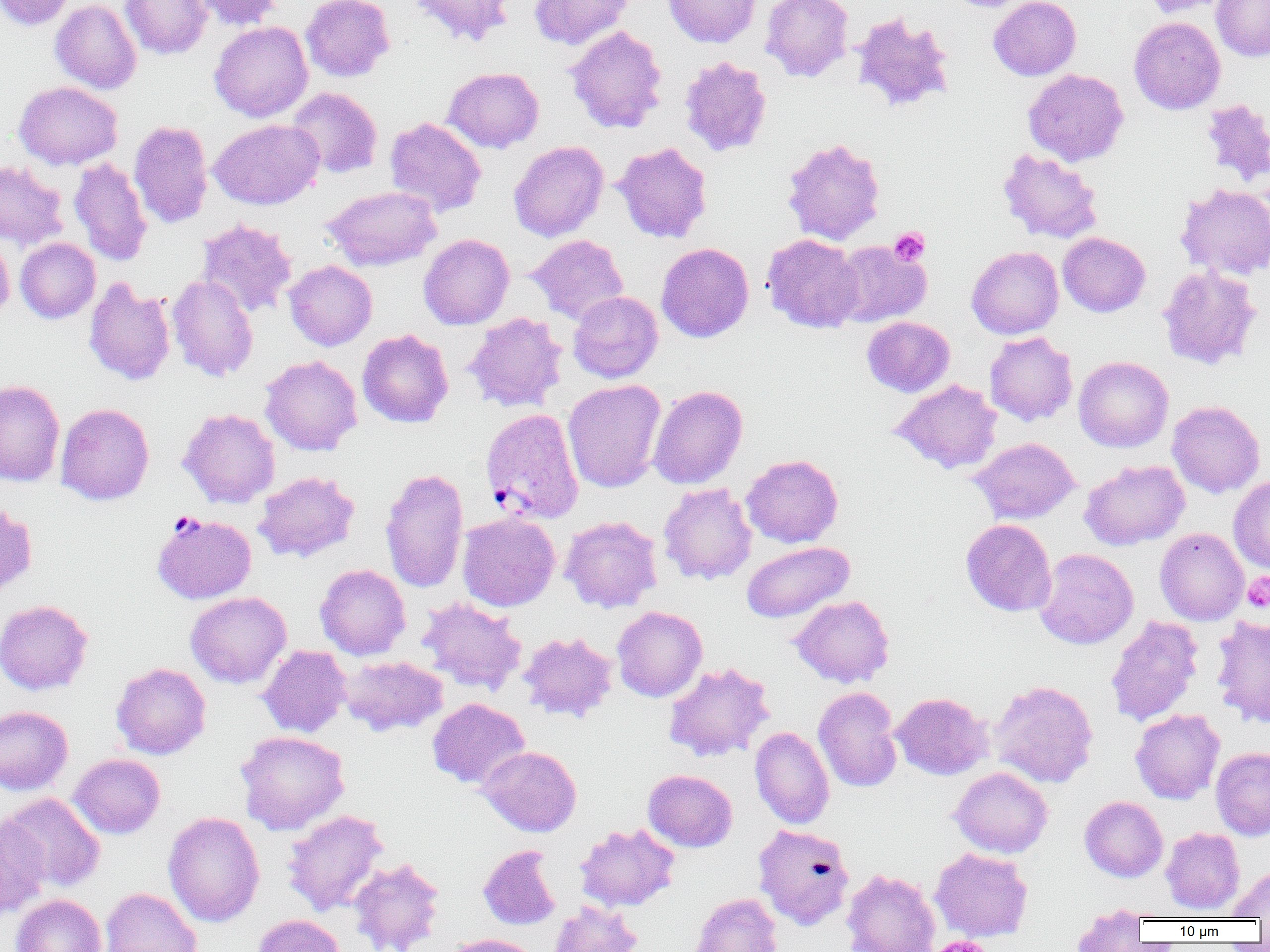

Summary:
  - Coordinate format: approximate bounding boxes as (x1, y1, x2, y2) in pixels
  - Plasmodium vivax-infected red blood cell locations: (480, 407, 585, 524), (151, 512, 257, 604)
  - Uninfected red blood cell locations: (1, 0, 76, 30), (50, 0, 142, 93), (120, 0, 212, 60), (190, 0, 284, 30), (300, 0, 395, 82), (408, 0, 514, 47), (529, 0, 636, 50), (663, 0, 761, 48), (761, 0, 854, 81), (948, 0, 1031, 12), (989, 0, 1081, 80), (1141, 0, 1233, 18), (1211, 0, 1270, 61), (851, 12, 956, 114), (1129, 16, 1226, 114), (209, 21, 313, 122), (565, 25, 668, 134), (679, 56, 772, 157), (443, 67, 544, 153), (1023, 69, 1128, 166), (14, 81, 123, 170), (287, 87, 383, 178), (1200, 98, 1270, 188), (384, 117, 486, 217), (209, 119, 324, 209), (129, 120, 213, 228), (782, 138, 886, 245), (509, 141, 609, 242), (612, 141, 712, 243), (997, 148, 1103, 244), (69, 157, 153, 265), (0, 160, 68, 250), (1176, 184, 1270, 280), (322, 186, 441, 271), (196, 218, 297, 318), (0, 232, 14, 324), (1058, 232, 1151, 317), (419, 233, 514, 329), (527, 234, 629, 324), (762, 234, 863, 333), (15, 238, 100, 323), (831, 240, 931, 328), (656, 242, 754, 342), (966, 246, 1063, 339), (284, 260, 377, 350), (1157, 265, 1262, 370), (167, 275, 259, 382), (83, 276, 176, 386), (568, 291, 663, 383), (463, 312, 568, 412), (862, 316, 955, 397), (357, 329, 454, 428), (984, 332, 1078, 426), (260, 355, 362, 456), (1074, 356, 1173, 452), (563, 379, 666, 492), (890, 379, 1003, 474), (0, 380, 65, 486), (648, 385, 748, 489), (1167, 401, 1265, 497), (55, 403, 154, 505), (178, 408, 280, 508), (968, 437, 1080, 524), (741, 454, 843, 548), (1080, 459, 1190, 550), (380, 467, 469, 592), (253, 471, 360, 563), (1229, 476, 1270, 573), (658, 483, 757, 585), (0, 502, 37, 597), (457, 512, 560, 611), (560, 515, 662, 613), (961, 519, 1057, 617), (1155, 527, 1249, 625), (741, 541, 854, 623), (1034, 548, 1139, 649), (315, 564, 411, 660), (185, 591, 291, 688), (789, 595, 895, 688), (417, 597, 527, 696), (0, 599, 93, 695), (612, 606, 707, 702), (1105, 615, 1203, 727), (1210, 615, 1270, 727), (517, 631, 618, 723), (257, 645, 351, 738), (340, 655, 448, 736), (662, 661, 774, 762), (111, 662, 211, 759), (989, 680, 1098, 788), (813, 687, 903, 792), (891, 692, 992, 780), (427, 698, 530, 788), (2, 705, 81, 891), (0, 706, 73, 795), (1130, 708, 1225, 804), (750, 727, 834, 829), (235, 730, 350, 835), (477, 746, 581, 836), (1210, 747, 1270, 840), (69, 754, 166, 839), (949, 767, 1053, 858), (643, 770, 737, 852), (1, 793, 105, 893), (1080, 796, 1168, 882), (282, 809, 389, 917), (163, 811, 265, 928), (0, 817, 50, 919), (575, 823, 680, 911), (753, 823, 855, 930), (1161, 827, 1245, 914), (478, 845, 561, 930), (930, 848, 1033, 942), (348, 857, 445, 952), (1229, 865, 1270, 920), (841, 868, 941, 952), (100, 887, 202, 952), (10, 893, 107, 952), (689, 893, 783, 952), (549, 900, 642, 952), (1071, 905, 1150, 950), (253, 914, 346, 952), (447, 934, 541, 952)
  - Platelet locations: (889, 227, 930, 266), (1242, 573, 1270, 613), (928, 936, 993, 952)
  - Slide-level diagnosis: Plasmodium vivax
  - Magnification: 1000x
  - Image size: 1270×952 pixels
  - Field of view: single
  - Preparation: thin blood film
  - Modality: light microscopy